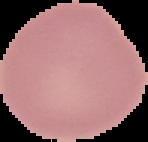
result = no malaria parasites seen
preparation = thin blood smear
image size = 148×142 pixels
image type = segmented cell region on a black background